Give the extent of all Plasmodium falciparum-infected red blood cells.
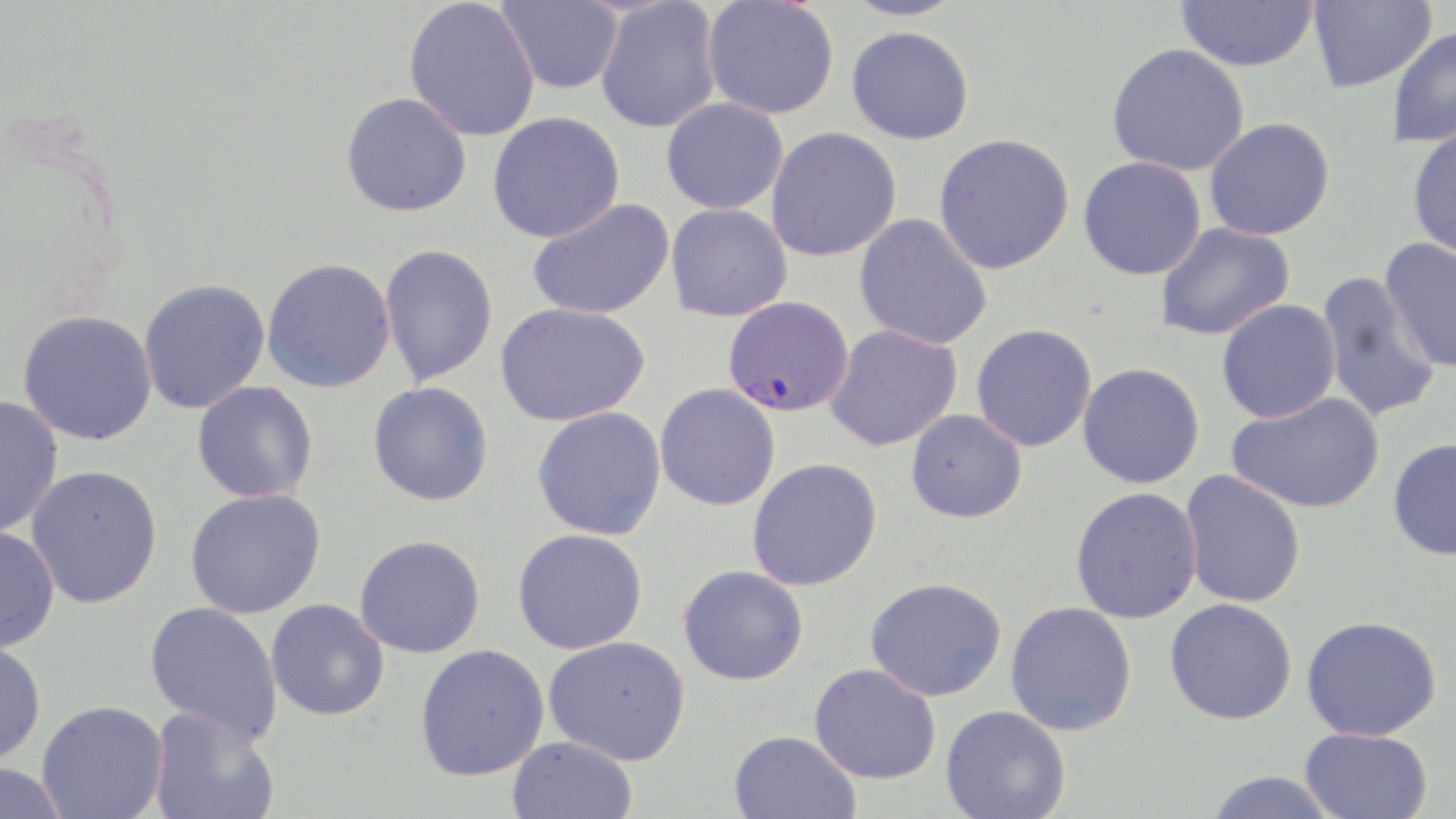
Approximate bounding boxes as (x1, y1, x2, y2) in pixels.
Plasmodium falciparum-infected red blood cells: (722, 296, 853, 417).

{
  "slide_level_diagnosis": "Plasmodium falciparum",
  "modality": "light microscopy",
  "field_of_view": "one of a larger specimen",
  "image_size": "1456×819 pixels",
  "magnification": "1000x",
  "stain": "May-Grünwald-Giemsa",
  "uninfected_red_blood_cell_locations": "approximate bounding boxes as (x1, y1, x2, y2) in pixels: (404, 0, 540, 142), (496, 0, 624, 94), (702, 0, 839, 119), (841, 0, 969, 21), (1176, 0, 1318, 71), (1308, 0, 1436, 93), (596, 1, 722, 133), (1387, 25, 1456, 150), (846, 26, 975, 145), (1107, 43, 1250, 176), (341, 92, 472, 217), (661, 98, 788, 214), (487, 111, 625, 243), (1204, 118, 1336, 241), (1407, 123, 1456, 261), (766, 127, 902, 262), (934, 133, 1075, 274), (1078, 156, 1207, 280), (527, 198, 675, 320), (666, 203, 793, 322), (854, 213, 992, 351), (1155, 222, 1295, 341), (1379, 237, 1456, 375), (379, 243, 499, 386), (262, 257, 396, 393), (1315, 270, 1443, 423), (138, 278, 270, 414), (1217, 299, 1341, 423), (495, 302, 650, 426), (17, 310, 157, 446), (971, 323, 1097, 452), (825, 324, 963, 451), (1078, 362, 1205, 488), (192, 380, 318, 503), (368, 382, 494, 506), (655, 383, 781, 511), (1227, 391, 1385, 514), (0, 395, 63, 538), (532, 406, 667, 540), (906, 409, 1028, 523), (1387, 437, 1456, 561), (746, 458, 883, 591), (25, 465, 163, 609), (1180, 470, 1306, 608), (1070, 486, 1203, 623), (185, 488, 326, 618), (0, 525, 60, 653), (513, 528, 647, 654), (354, 534, 486, 658), (678, 564, 808, 685), (865, 577, 1007, 702), (266, 598, 390, 721), (1165, 598, 1297, 725), (1005, 601, 1137, 736), (145, 602, 283, 745), (1302, 615, 1442, 741), (544, 636, 691, 765), (0, 640, 47, 768), (415, 643, 550, 781), (809, 663, 941, 784), (36, 700, 169, 819), (941, 705, 1071, 819), (148, 708, 280, 819), (1300, 727, 1433, 818), (729, 730, 861, 819), (507, 736, 639, 819), (0, 762, 70, 819), (1204, 771, 1340, 819)",
  "preparation": "thin blood smear"
}